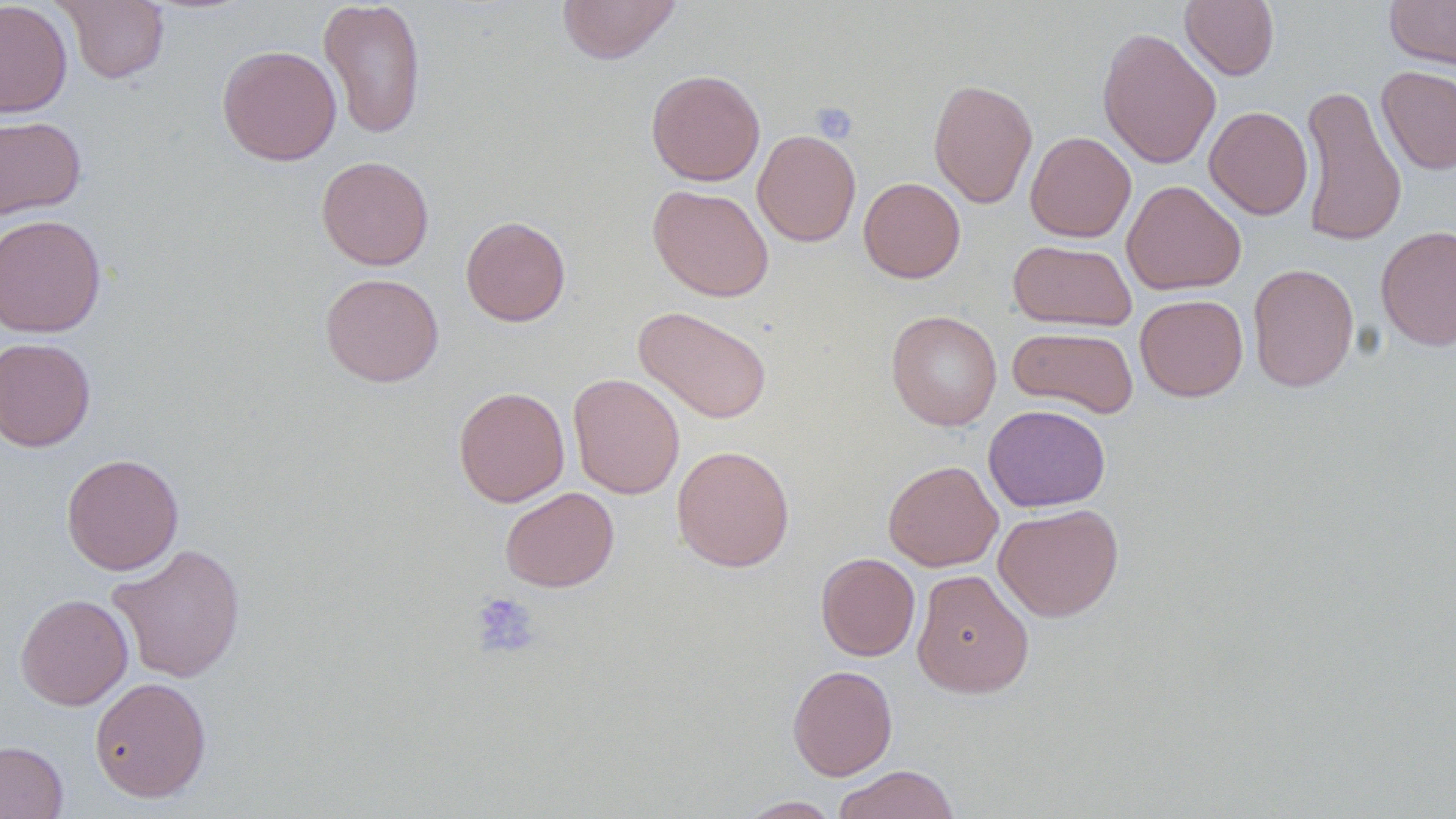 Approximate bounding boxes as [x1, y1, x2, y2] in pixels. Uninfected red blood cell locations: [0, 0, 72, 118], [56, 0, 169, 84], [318, 0, 427, 139], [556, 0, 682, 64], [1384, 0, 1456, 70], [1180, 1, 1279, 80], [1096, 26, 1221, 169], [217, 45, 342, 166], [1377, 66, 1456, 175], [645, 69, 766, 186], [928, 78, 1038, 208], [1298, 84, 1408, 247], [1204, 105, 1313, 220], [0, 114, 86, 220], [753, 129, 861, 247], [1025, 131, 1137, 242], [316, 155, 434, 270], [858, 177, 965, 283], [1122, 179, 1246, 295], [648, 184, 774, 302], [1, 214, 106, 338], [460, 215, 571, 326], [1375, 225, 1456, 352], [1008, 239, 1137, 331], [1247, 263, 1359, 392], [320, 272, 444, 387], [1135, 294, 1249, 401], [634, 306, 773, 424], [886, 310, 1003, 430], [1007, 326, 1139, 418], [0, 336, 96, 452], [568, 373, 685, 499], [453, 386, 570, 507], [983, 404, 1111, 512], [672, 444, 795, 572], [61, 453, 184, 576], [883, 460, 1003, 571], [499, 487, 619, 592], [993, 503, 1124, 622], [107, 543, 247, 683], [816, 553, 920, 661], [911, 569, 1035, 698], [15, 593, 133, 710], [787, 664, 897, 780], [89, 677, 212, 802], [0, 740, 69, 819], [831, 764, 961, 819], [737, 796, 842, 818]. Platelet locations: [811, 101, 859, 143], [470, 592, 541, 659]. Slide-level diagnosis: no evidence of blood parasites. Single field of view. Thin blood smear. Image is 1456×819 pixels. Optical microscopy. Captured at 1000x magnification. May-Grünwald-Giemsa-stained preparation.